Report the malaria status of this cell.
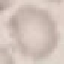
Uninfected.

Summary:
  - Image type: automatically extracted cell patch, resized to 64 × 64 pixels
  - Stain: Giemsa
  - Preparation: thin smear
  - Capture: smartphone through the microscope eyepiece